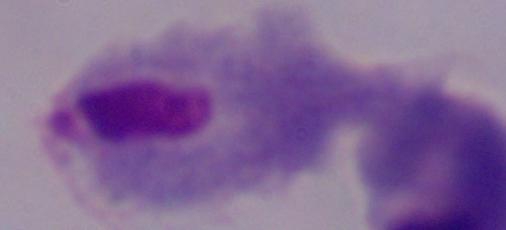

modality = micrograph
magnification = 1000x
identification = trichomonad